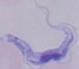
{
  "identification": "trypanosome",
  "modality": "micrograph",
  "magnification": "1000x"
}